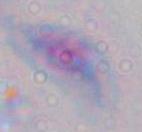
Summary:
  - Identification: Toxoplasma gondii
  - Modality: photomicrograph
  - Magnification: 1000x